Give the extent of all Plasmodium falciparum-infected red blood cells.
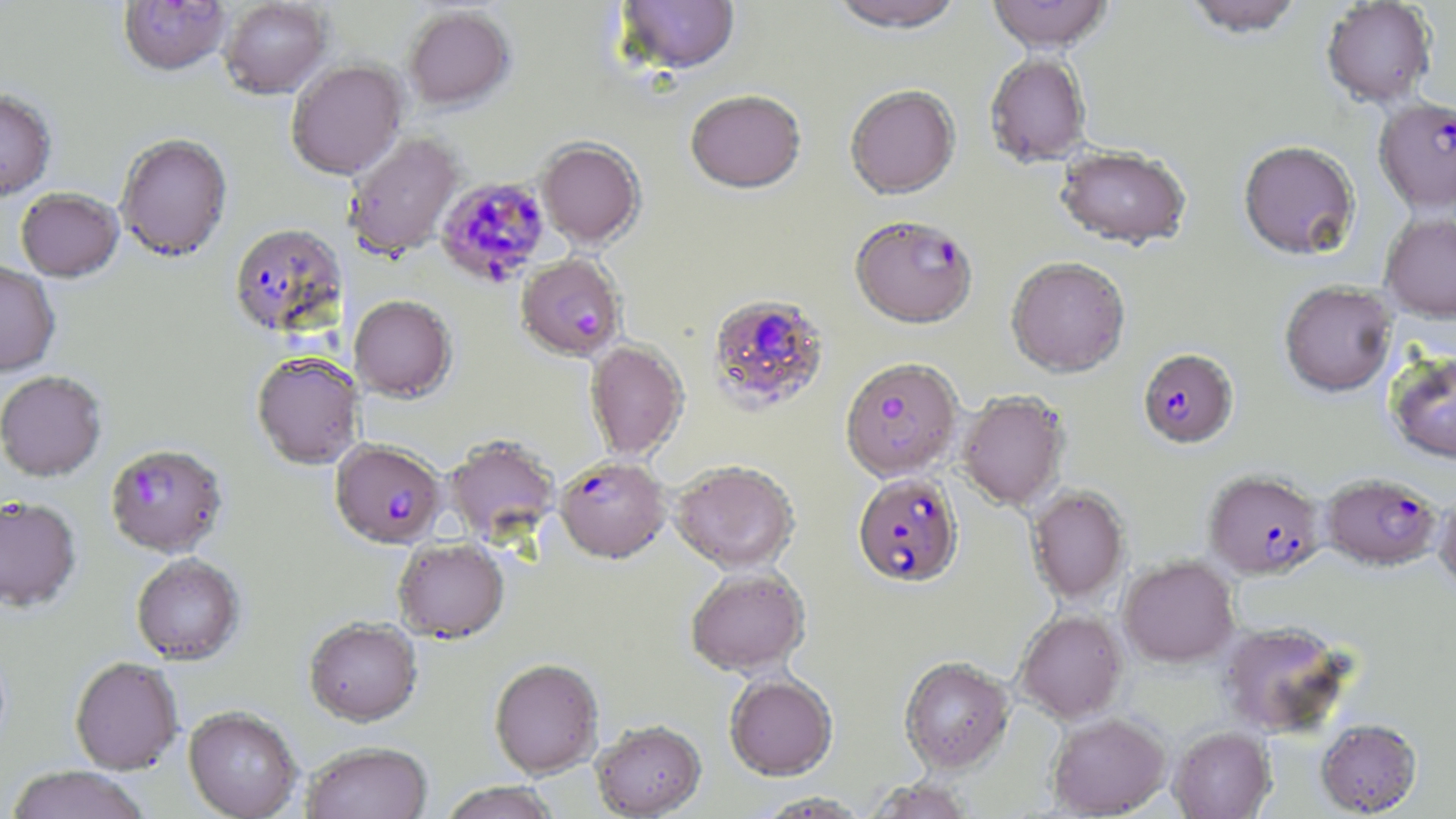
Approximate bounding boxes as named x1/y1/x2/y2 corners in pixels.
Plasmodium falciparum-infected red blood cells: (x1=1373, y1=100, x2=1456, y2=216), (x1=434, y1=178, x2=551, y2=288), (x1=850, y1=218, x2=978, y2=332), (x1=229, y1=225, x2=347, y2=341), (x1=516, y1=256, x2=625, y2=364), (x1=708, y1=294, x2=829, y2=413), (x1=1137, y1=348, x2=1239, y2=450), (x1=840, y1=359, x2=962, y2=484), (x1=330, y1=441, x2=446, y2=552), (x1=105, y1=446, x2=227, y2=560), (x1=555, y1=459, x2=671, y2=567), (x1=1203, y1=472, x2=1325, y2=582), (x1=852, y1=473, x2=964, y2=589), (x1=1322, y1=475, x2=1441, y2=573).

slide-level diagnosis = Plasmodium falciparum
preparation = thin blood smear
magnification = 1000x
modality = optical microscopy
stain = May-Grünwald-Giemsa
image size = 1456×819 pixels
field of view = one of a larger specimen
uninfected red blood cell locations = approximate bounding boxes as named x1/y1/x2/y2 corners in pixels: (x1=615, y1=0, x2=740, y2=78), (x1=828, y1=0, x2=964, y2=37), (x1=986, y1=0, x2=1113, y2=55), (x1=1182, y1=0, x2=1306, y2=42), (x1=118, y1=1, x2=231, y2=79), (x1=220, y1=1, x2=332, y2=101), (x1=1321, y1=1, x2=1436, y2=109), (x1=404, y1=8, x2=515, y2=114), (x1=984, y1=54, x2=1092, y2=169), (x1=286, y1=61, x2=409, y2=182), (x1=845, y1=86, x2=960, y2=201), (x1=0, y1=92, x2=57, y2=204), (x1=685, y1=92, x2=806, y2=197), (x1=345, y1=133, x2=464, y2=261), (x1=116, y1=135, x2=233, y2=265), (x1=537, y1=141, x2=644, y2=251), (x1=1238, y1=144, x2=1360, y2=263), (x1=1055, y1=148, x2=1192, y2=252), (x1=16, y1=190, x2=124, y2=284), (x1=1380, y1=213, x2=1456, y2=325), (x1=1006, y1=257, x2=1130, y2=379), (x1=0, y1=264, x2=60, y2=379), (x1=1280, y1=282, x2=1397, y2=399), (x1=349, y1=296, x2=457, y2=404), (x1=584, y1=342, x2=688, y2=462), (x1=1385, y1=352, x2=1456, y2=466), (x1=251, y1=355, x2=364, y2=471), (x1=0, y1=373, x2=107, y2=483), (x1=958, y1=391, x2=1069, y2=511), (x1=444, y1=438, x2=559, y2=546), (x1=669, y1=463, x2=800, y2=577), (x1=1027, y1=486, x2=1130, y2=604), (x1=1434, y1=486, x2=1456, y2=594), (x1=0, y1=500, x2=81, y2=615), (x1=393, y1=541, x2=509, y2=645), (x1=131, y1=556, x2=245, y2=667), (x1=1119, y1=558, x2=1239, y2=668), (x1=686, y1=570, x2=810, y2=679), (x1=1015, y1=611, x2=1128, y2=724), (x1=304, y1=619, x2=423, y2=729), (x1=1219, y1=622, x2=1353, y2=738), (x1=70, y1=659, x2=184, y2=775), (x1=899, y1=659, x2=1014, y2=775), (x1=489, y1=661, x2=604, y2=781), (x1=724, y1=676, x2=838, y2=782), (x1=183, y1=708, x2=303, y2=819), (x1=1047, y1=714, x2=1171, y2=818), (x1=1315, y1=719, x2=1423, y2=817), (x1=591, y1=724, x2=707, y2=819), (x1=1169, y1=727, x2=1275, y2=819), (x1=302, y1=743, x2=433, y2=819), (x1=3, y1=767, x2=151, y2=819), (x1=864, y1=780, x2=976, y2=819), (x1=439, y1=783, x2=560, y2=819), (x1=756, y1=793, x2=870, y2=818)